Find each WBC.
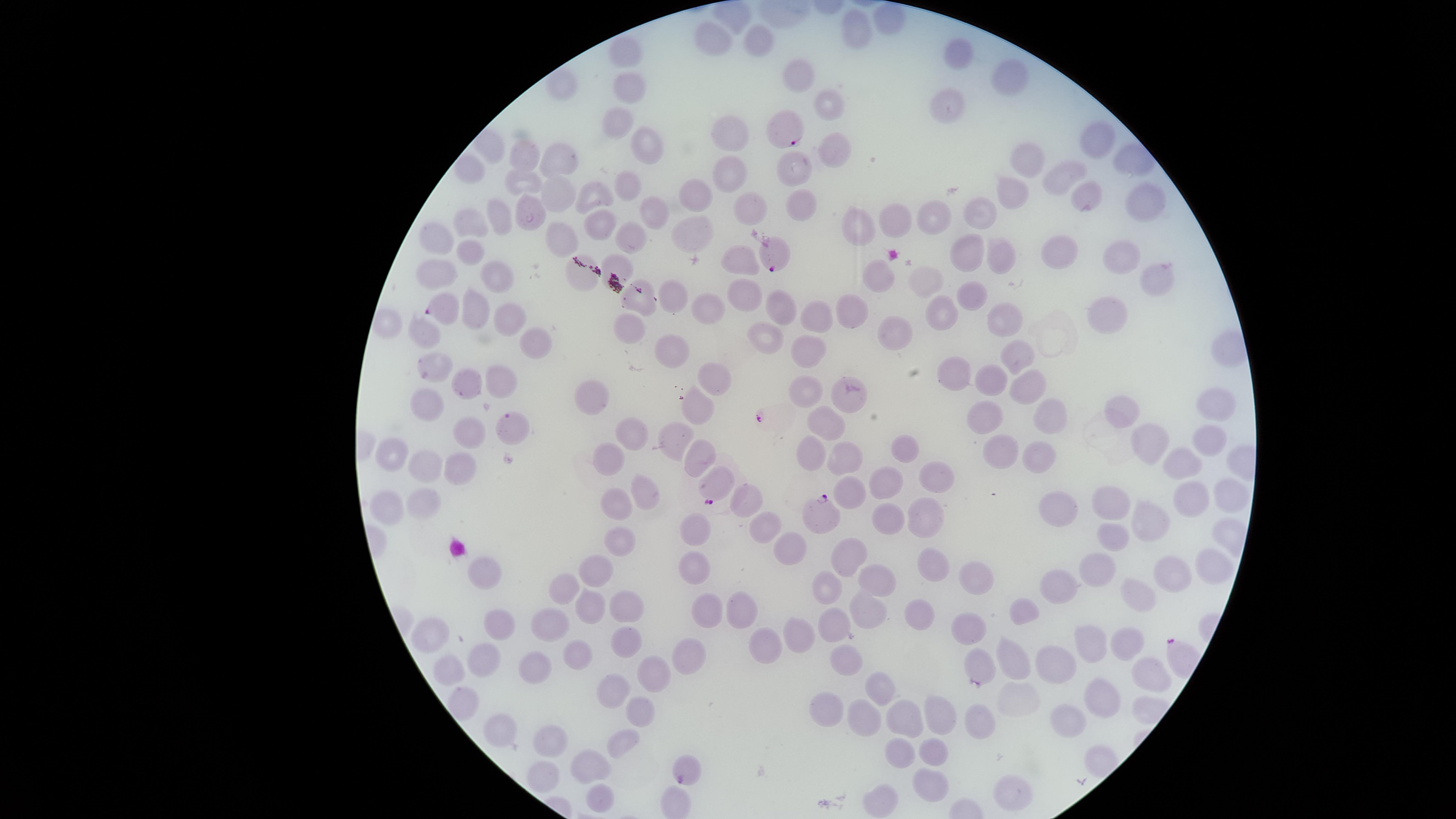
No WBCs identified.

Approximate marker points, in pixels from the top-left corner.
Summary:
  - Parasitized RBCs: (x=783, y=126), (x=775, y=258), (x=442, y=308), (x=512, y=426), (x=822, y=512), (x=685, y=773)
  - Uninfected RBCs: (x=886, y=24), (x=709, y=33), (x=862, y=35), (x=762, y=36), (x=627, y=48), (x=959, y=57), (x=803, y=71), (x=1000, y=80), (x=560, y=84), (x=630, y=85), (x=828, y=107), (x=948, y=107), (x=616, y=120), (x=730, y=135), (x=1097, y=142), (x=490, y=145), (x=833, y=145), (x=645, y=149), (x=525, y=152), (x=558, y=158), (x=1128, y=160), (x=1028, y=165), (x=470, y=169), (x=801, y=170), (x=729, y=171), (x=525, y=178), (x=1061, y=178), (x=595, y=189), (x=629, y=191), (x=559, y=192), (x=1012, y=196), (x=697, y=197), (x=1086, y=197), (x=1137, y=201), (x=527, y=206), (x=750, y=206), (x=803, y=207), (x=654, y=213), (x=981, y=215), (x=934, y=216), (x=500, y=217), (x=891, y=221), (x=471, y=222), (x=601, y=224), (x=854, y=227), (x=629, y=233), (x=436, y=236), (x=694, y=238), (x=472, y=248), (x=1059, y=249), (x=972, y=252), (x=1000, y=256), (x=1120, y=259), (x=745, y=262), (x=622, y=265), (x=440, y=270), (x=578, y=274), (x=495, y=276), (x=882, y=276), (x=927, y=276), (x=1158, y=276), (x=974, y=293), (x=743, y=295), (x=672, y=299), (x=645, y=304), (x=479, y=306), (x=709, y=306), (x=778, y=309), (x=819, y=310), (x=943, y=310), (x=1103, y=313), (x=848, y=315), (x=505, y=317), (x=995, y=317), (x=889, y=331), (x=423, y=333), (x=630, y=334), (x=765, y=335), (x=531, y=341), (x=676, y=343), (x=814, y=345), (x=1017, y=355), (x=438, y=362), (x=951, y=370), (x=714, y=373), (x=502, y=375), (x=471, y=379), (x=994, y=381), (x=1025, y=386), (x=807, y=390), (x=599, y=399), (x=690, y=399), (x=847, y=399), (x=426, y=404), (x=1218, y=404), (x=1122, y=407), (x=980, y=415), (x=1049, y=415), (x=827, y=420), (x=466, y=429), (x=630, y=436), (x=675, y=440), (x=1149, y=441), (x=1210, y=442), (x=898, y=448), (x=1003, y=448), (x=388, y=452), (x=813, y=452), (x=701, y=457), (x=1040, y=457), (x=842, y=459), (x=611, y=462), (x=1184, y=463), (x=424, y=466), (x=458, y=471), (x=936, y=474), (x=723, y=475), (x=887, y=483), (x=855, y=486), (x=1198, y=490), (x=1230, y=492), (x=644, y=494), (x=1112, y=499), (x=752, y=502), (x=1066, y=503), (x=386, y=505), (x=422, y=505), (x=616, y=507), (x=920, y=516), (x=889, y=518), (x=1155, y=518), (x=762, y=523), (x=697, y=526), (x=1114, y=533), (x=620, y=535), (x=786, y=545), (x=846, y=548), (x=1220, y=561), (x=933, y=562), (x=1095, y=565), (x=1176, y=565), (x=696, y=568), (x=595, y=570), (x=489, y=572), (x=881, y=574), (x=973, y=576), (x=1056, y=580), (x=564, y=583), (x=829, y=583), (x=1138, y=589), (x=624, y=598), (x=584, y=606), (x=705, y=608), (x=864, y=608), (x=1028, y=608), (x=747, y=612), (x=921, y=615), (x=551, y=621), (x=835, y=622), (x=500, y=626), (x=970, y=627), (x=434, y=632), (x=797, y=636), (x=1127, y=639), (x=1090, y=640), (x=623, y=641), (x=765, y=647), (x=571, y=652), (x=1007, y=653), (x=687, y=655), (x=846, y=658), (x=1059, y=659), (x=481, y=660), (x=980, y=660), (x=533, y=666), (x=653, y=667), (x=1147, y=670), (x=445, y=673), (x=619, y=680), (x=881, y=684), (x=1101, y=697), (x=822, y=705), (x=462, y=707), (x=902, y=713), (x=939, y=713), (x=1064, y=715), (x=643, y=717), (x=862, y=717), (x=983, y=722), (x=493, y=726), (x=624, y=737), (x=553, y=743), (x=898, y=748), (x=939, y=751), (x=585, y=768), (x=936, y=777), (x=540, y=783), (x=1006, y=788), (x=598, y=794), (x=882, y=795), (x=677, y=800)
  - Presence: malaria parasites detected
  - Image size: 1456×819 pixels
  - Preparation: thin smear of blood
  - Field of view: single
  - Species: Plasmodium falciparum
  - Stain: Giemsa
  - Visible region: circular
  - Capture: smartphone photograph through the microscope eyepiece